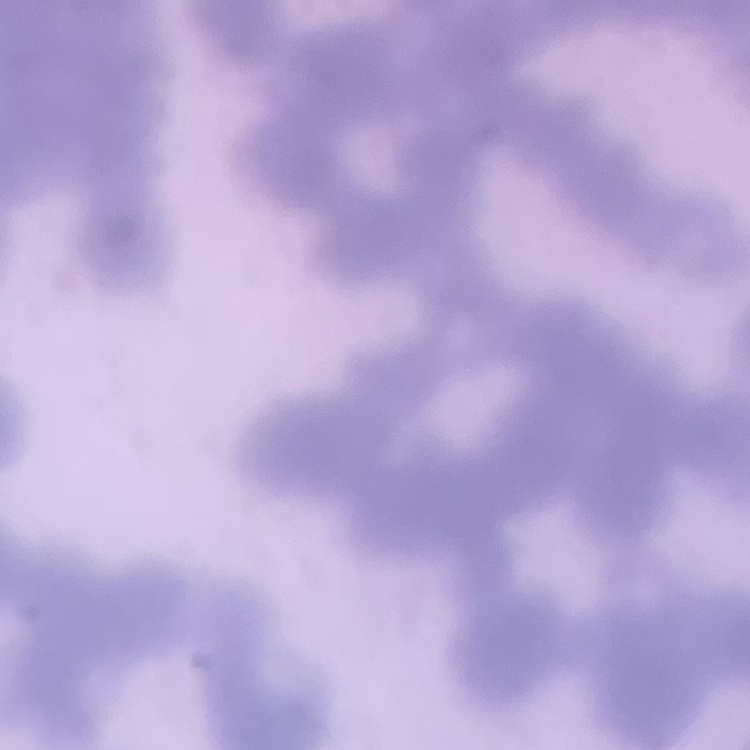
{
  "red_blood_cell_morphology": "rouleaux formation",
  "image_type": "one tile cut from a larger photomicrograph",
  "preparation": "thin blood smear",
  "stain": "Field's or Giemsa"
}